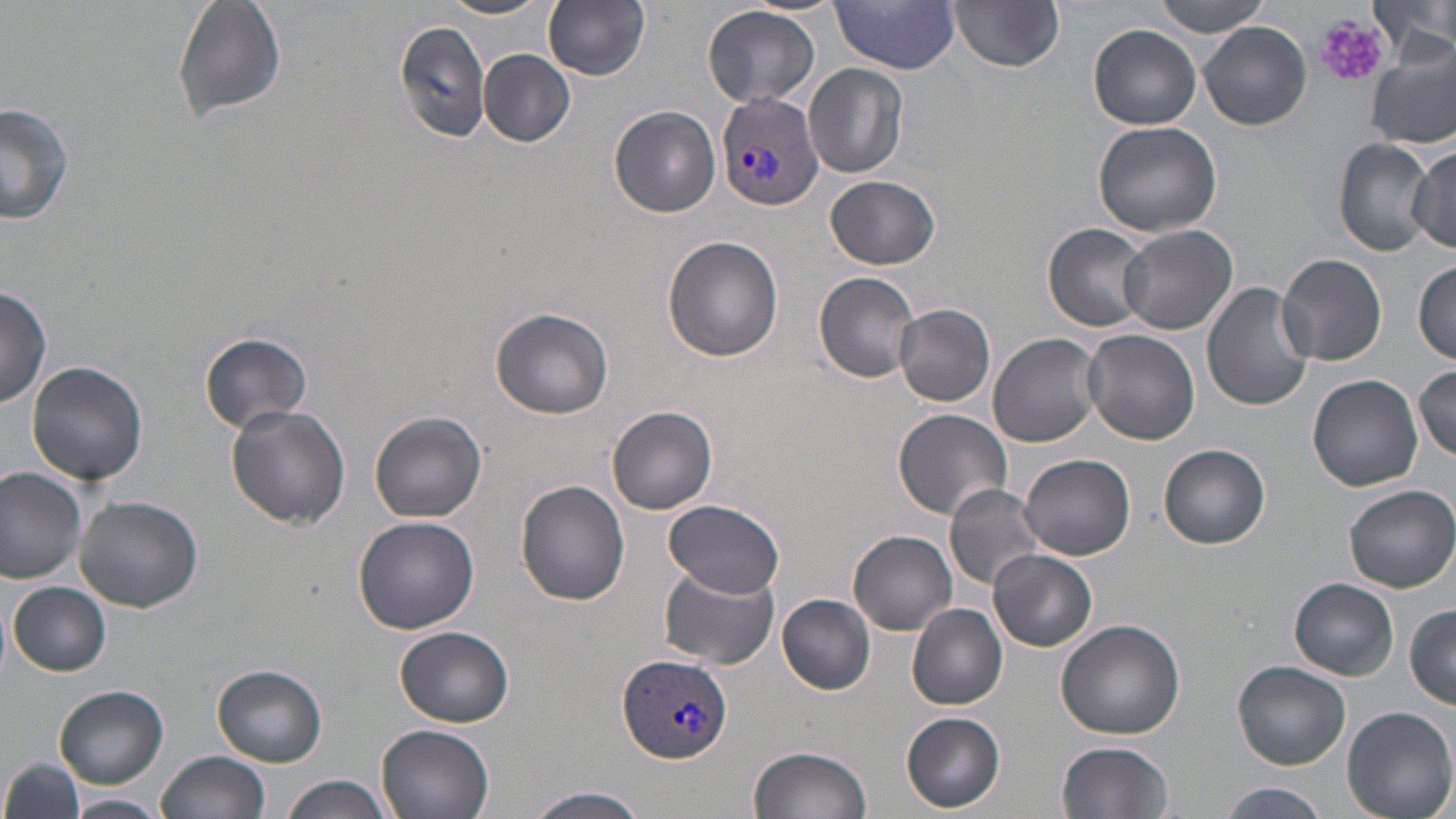
Approximate bounding boxes as (x1, y1, x2, y2) in pixels. Platelet locations: (1315, 15, 1389, 89). Uninfected red blood cell locations: (172, 0, 287, 123), (438, 0, 552, 20), (544, 0, 652, 80), (1151, 0, 1274, 37), (1374, 0, 1454, 69), (833, 1, 962, 73), (948, 1, 1066, 72), (703, 4, 821, 109), (393, 18, 493, 143), (1200, 22, 1312, 131), (1090, 25, 1202, 129), (1366, 42, 1455, 149), (479, 49, 575, 147), (805, 65, 910, 179), (0, 102, 74, 226), (610, 107, 721, 217), (1093, 121, 1223, 238), (1334, 138, 1435, 254), (1409, 147, 1455, 253), (826, 174, 941, 269), (1044, 223, 1155, 331), (1115, 224, 1237, 334), (663, 236, 784, 362), (1278, 254, 1388, 365), (1413, 260, 1455, 363), (815, 272, 920, 382), (1204, 282, 1317, 410), (0, 287, 50, 408), (895, 304, 995, 407), (491, 306, 613, 419), (1080, 328, 1200, 445), (199, 332, 312, 431), (987, 332, 1104, 447), (28, 360, 147, 484), (1412, 363, 1456, 464), (1309, 374, 1424, 493), (607, 403, 717, 515), (226, 405, 351, 530), (894, 410, 1013, 522), (371, 412, 488, 524), (1158, 443, 1269, 547), (1021, 453, 1136, 560), (0, 468, 86, 584), (516, 480, 630, 606), (943, 484, 1046, 592), (1345, 485, 1456, 592), (74, 495, 203, 610), (663, 499, 786, 599), (354, 516, 479, 633), (849, 531, 957, 634), (989, 550, 1096, 651), (659, 565, 779, 669), (1290, 578, 1397, 679), (9, 581, 111, 676), (776, 592, 876, 695), (1405, 604, 1456, 707), (907, 605, 1008, 710), (1056, 616, 1188, 738), (396, 625, 514, 726), (1234, 659, 1351, 769), (212, 665, 325, 765), (54, 686, 168, 788), (1341, 705, 1456, 819), (901, 712, 1006, 813), (377, 723, 496, 819), (1057, 740, 1175, 819), (748, 745, 870, 819), (157, 750, 270, 819), (2, 760, 84, 816), (282, 774, 393, 819), (1214, 783, 1332, 818), (520, 786, 651, 819), (65, 793, 172, 818). Plasmodium vivax-infected red blood cell locations: (715, 90, 823, 212), (619, 651, 733, 765). Slide-level diagnosis: Plasmodium vivax. Thin blood smear. May-Grünwald-Giemsa stain. Single field of view. Image is 1456×819 pixels. Optical microscopy. 1000x magnification.